Point out each leukocyte.
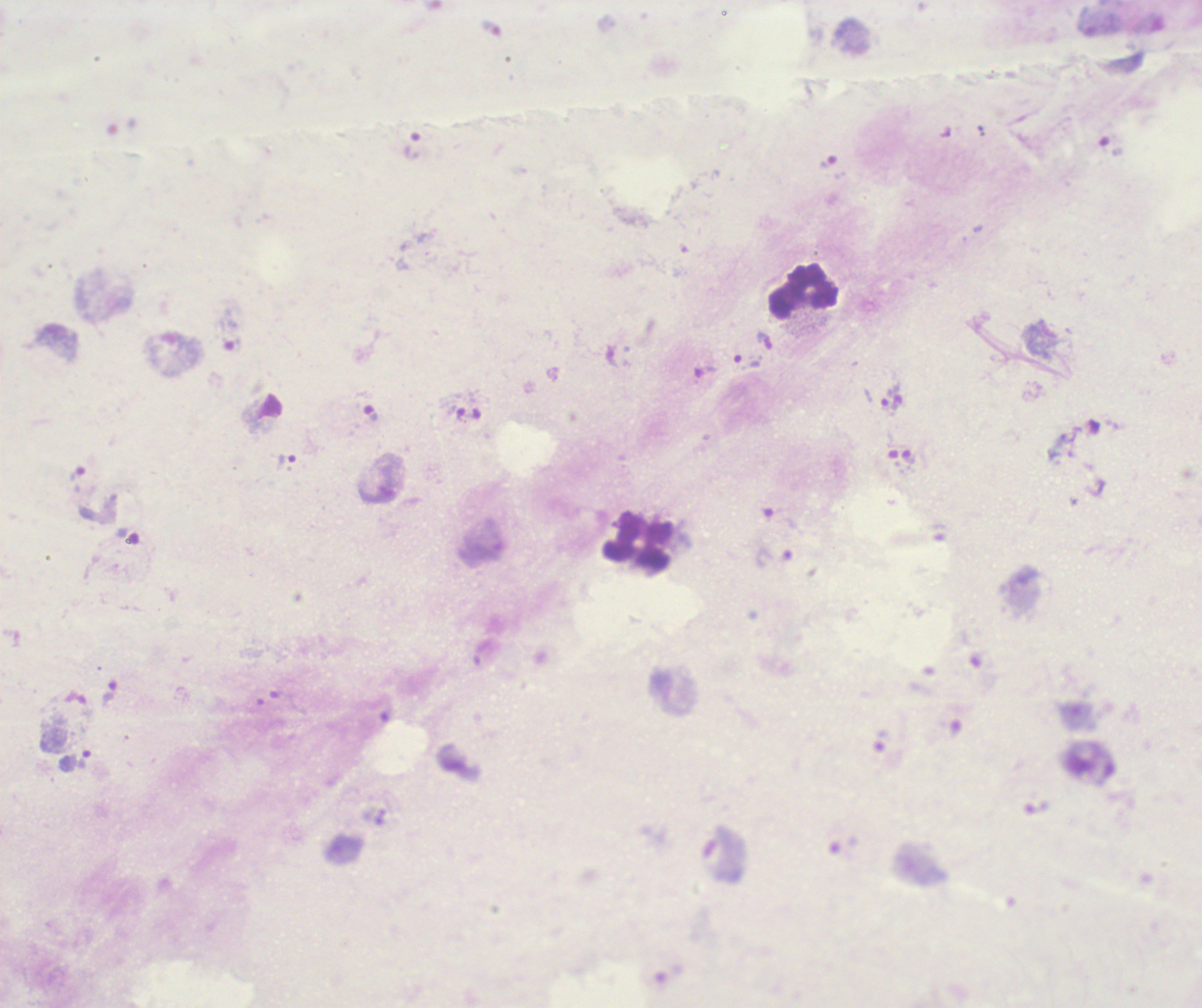

Approximate centers as {x, y} in pixels.
Leukocytes: {804, 291}, {637, 541}.

Approximate centers as {x, y} in pixels. Trophozoite locations: {413, 146}, {748, 361}, {704, 372}, {897, 393}, {887, 408}, {370, 413}, {287, 460}, {109, 693}, {83, 759}. Image is 1202×1008 pixels. Coloration quality: bad. Captured at 100x magnification. Result: malaria parasites identified. Romanowsky-stained preparation. Thick blood smear. Previously used in a real diagnosis. Single field of view. Background quality: poor.